Locate and identify every blood parasite.
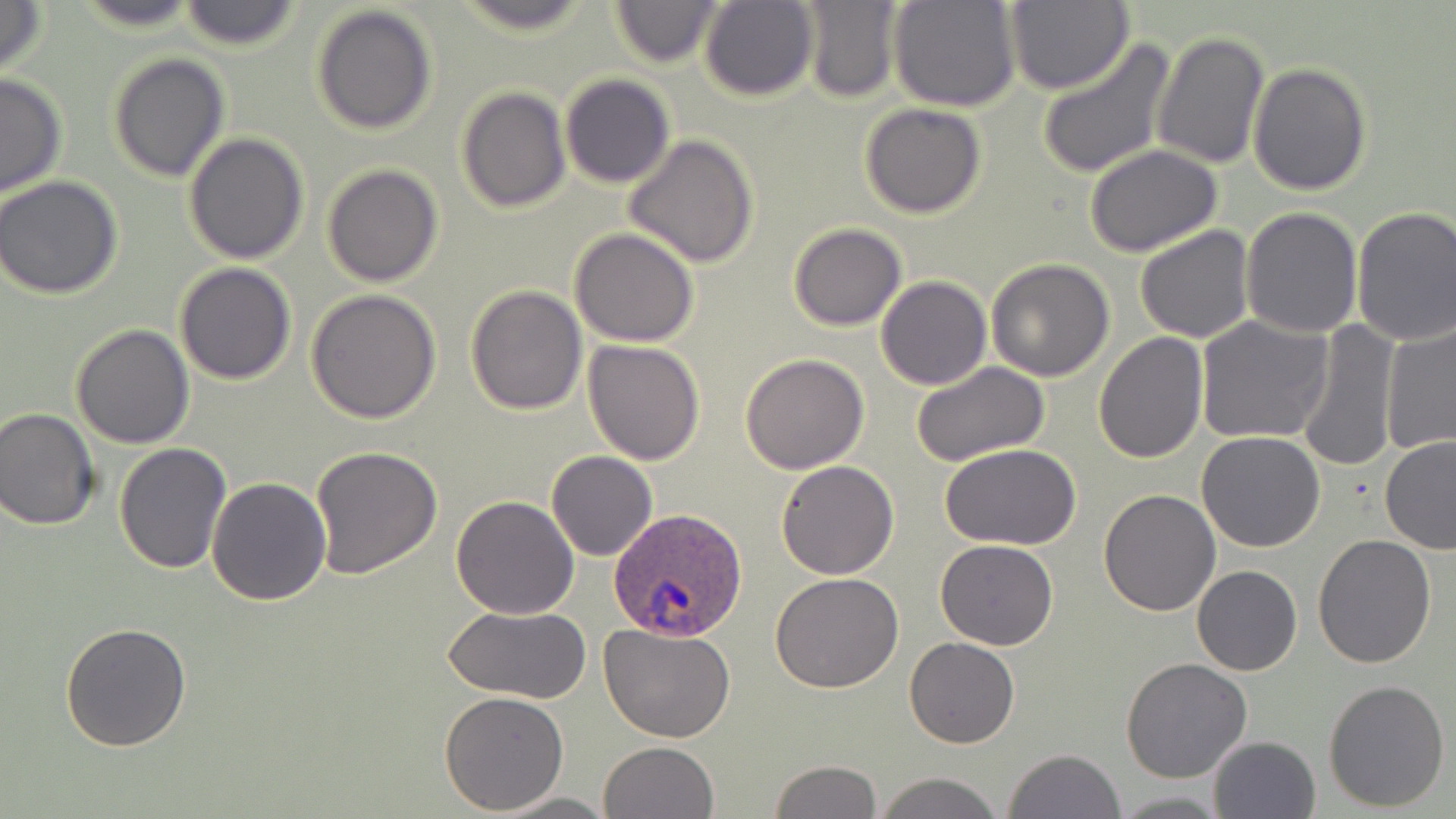

Approximate bounding boxes as (x1, y1, x2, y2) in pixels.
Plasmodium ovale-infected red blood cells: (609, 507, 746, 644).
No Plasmodium falciparum, Plasmodium malariae, Plasmodium vivax, Babesia divergens, or Trypanosoma brucei observed.

Uninfected red blood cell locations: (0, 0, 49, 80), (72, 0, 205, 29), (450, 0, 599, 37), (607, 0, 726, 68), (698, 0, 819, 102), (890, 0, 1021, 112), (178, 1, 305, 52), (800, 1, 903, 102), (1006, 1, 1133, 96), (311, 4, 439, 136), (1152, 29, 1269, 169), (1036, 38, 1175, 178), (107, 52, 230, 182), (1248, 62, 1372, 196), (0, 72, 68, 198), (560, 74, 674, 188), (457, 86, 571, 212), (859, 103, 986, 218), (184, 133, 311, 265), (623, 134, 759, 269), (1084, 146, 1224, 256), (322, 165, 443, 287), (0, 176, 124, 301), (1351, 205, 1456, 346), (1241, 207, 1365, 339), (786, 222, 908, 331), (1134, 225, 1255, 344), (569, 229, 700, 347), (985, 259, 1115, 382), (174, 263, 298, 385), (876, 275, 991, 390), (465, 284, 588, 414), (307, 290, 442, 426), (1195, 315, 1331, 446), (1293, 320, 1404, 472), (1380, 321, 1456, 455), (70, 323, 196, 448), (1094, 331, 1209, 464), (583, 339, 706, 465), (740, 353, 870, 474), (910, 360, 1051, 467), (1, 406, 101, 530), (1197, 431, 1326, 552), (1379, 435, 1456, 553), (114, 442, 232, 574), (939, 443, 1084, 549), (309, 445, 441, 579), (546, 451, 658, 561), (775, 459, 900, 579), (206, 478, 332, 605), (1098, 487, 1221, 615), (450, 496, 579, 619), (1312, 535, 1437, 669), (934, 538, 1059, 651), (1192, 564, 1302, 676), (770, 571, 905, 694), (442, 605, 590, 703), (61, 621, 193, 753), (599, 622, 736, 742), (905, 638, 1019, 749), (1120, 657, 1252, 783), (1323, 678, 1451, 813), (438, 690, 569, 813), (1208, 735, 1321, 819), (598, 741, 720, 819), (1004, 748, 1127, 819), (769, 760, 881, 818), (873, 772, 1005, 819), (1112, 791, 1226, 816), (494, 792, 615, 818). Slide-level diagnosis: Plasmodium ovale. Light microscopy. May-Grünwald-Giemsa stain. Image is 1456×819 pixels. Single field of view. Thin blood film. 1000x magnification.